Point out each Plasmodium parasite.
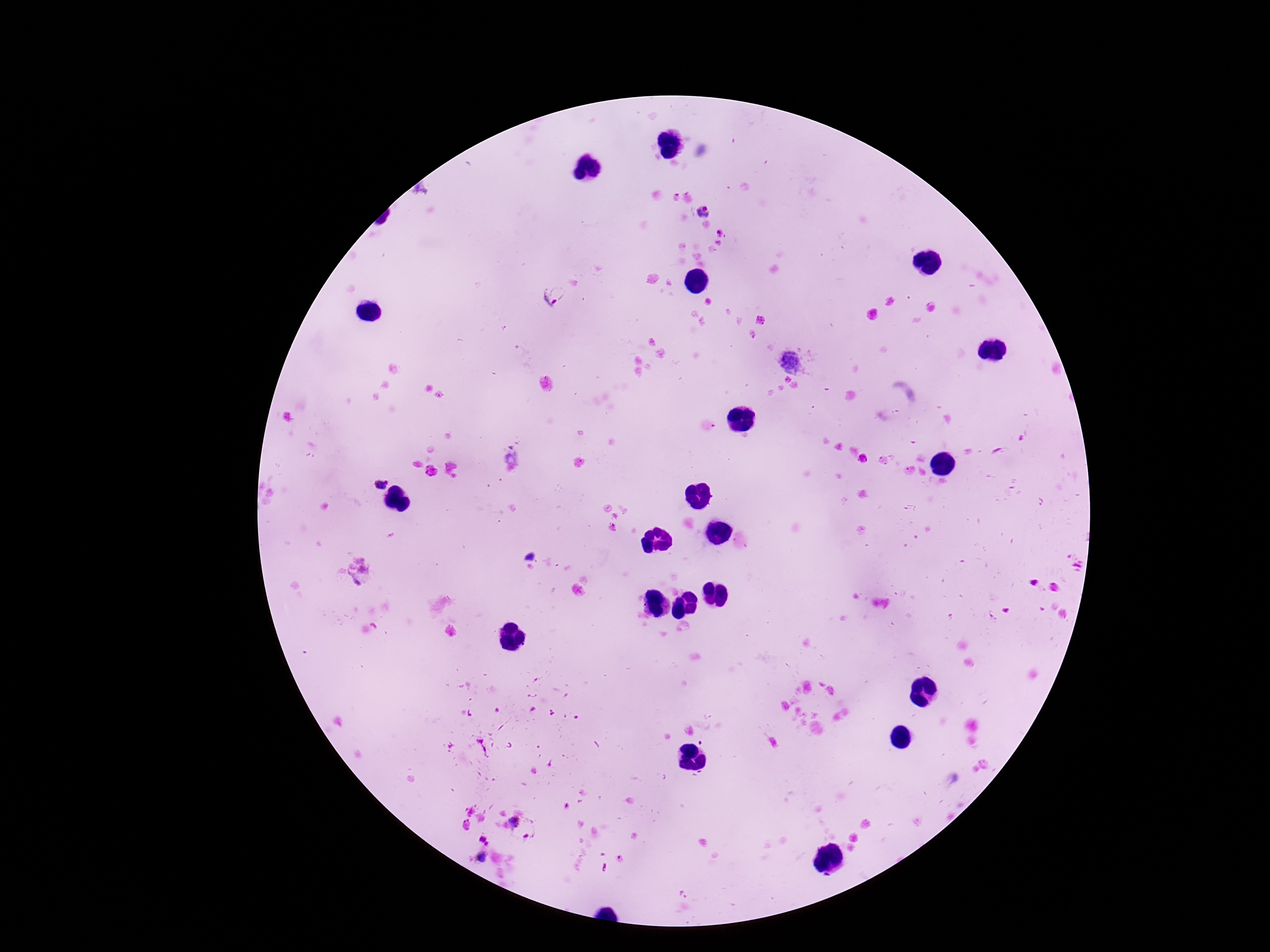

Approximate centers as [x, y] in pixels.
Plasmodium parasites: [702, 210], [555, 299], [792, 362], [380, 485], [515, 823], [482, 858].

Summary:
  - Stain: Giemsa
  - Image size: 1270×952 pixels
  - Field of view: one from this slide
  - Patient malaria status: infected
  - Capture: smartphone camera through the microscope eyepiece
  - Preparation: thick peripheral-blood smear
  - Magnification: 100x